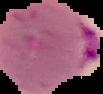

Summary:
  - Image size: 103×94 pixels
  - Result: Plasmodium parasites detected
  - Image type: cell region segmented out of the field of view; surrounding area masked to black
  - Preparation: thin blood film